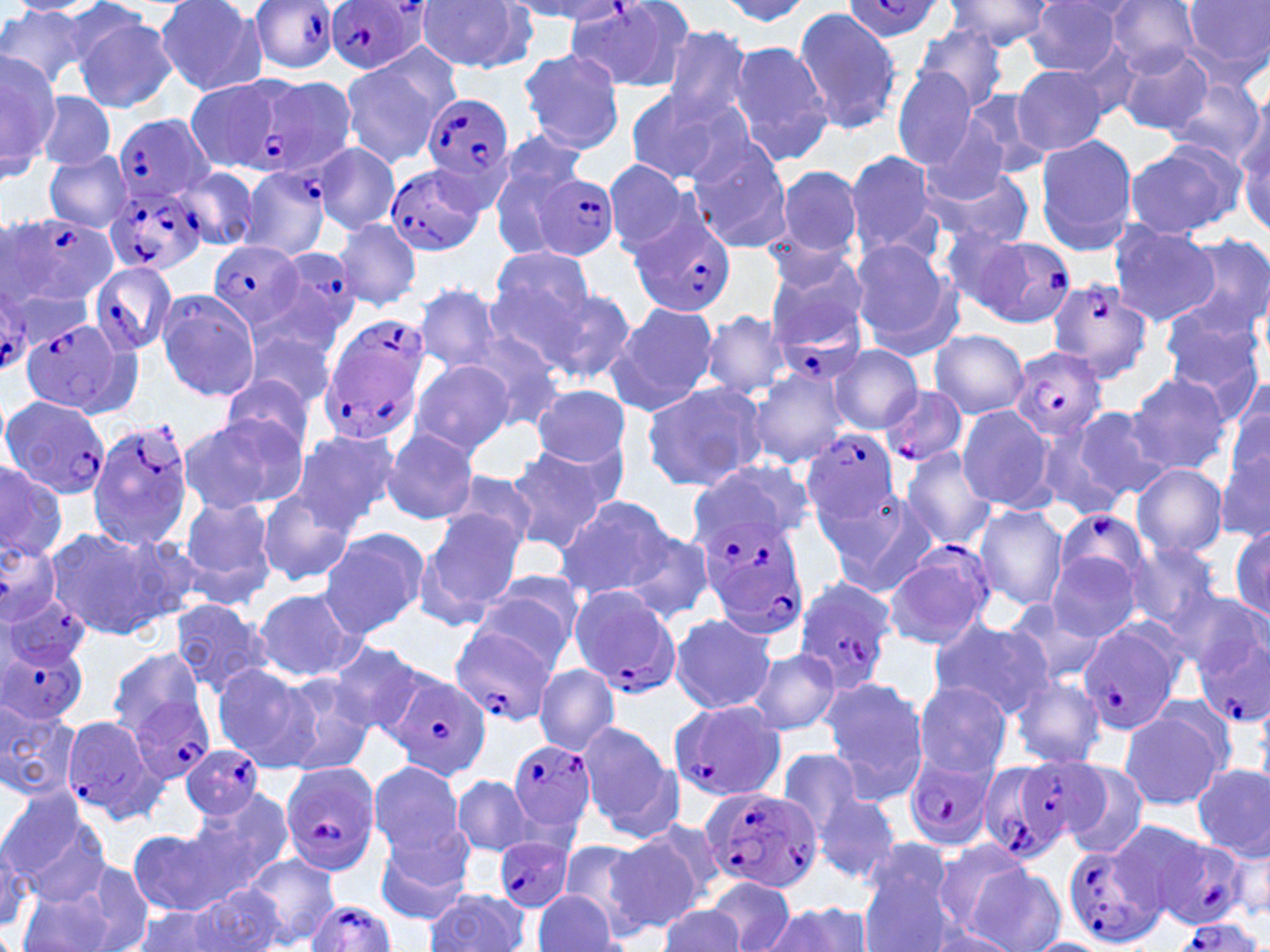
Summary:
  - Coordinate format: approximate bounding boxes as [x1, y1, x2, y2] in pixels
  - Plasmodium falciparum-infected red blood cell locations (subset): [568, 0, 699, 94], [247, 1, 342, 73], [325, 1, 426, 76], [842, 1, 946, 40], [221, 77, 317, 181], [423, 93, 513, 190], [110, 114, 217, 201], [386, 162, 488, 257], [239, 165, 332, 261], [534, 173, 621, 261], [101, 186, 203, 276], [630, 209, 735, 318], [10, 214, 117, 305], [951, 232, 1073, 326], [208, 241, 304, 331], [261, 246, 363, 353], [90, 262, 179, 356], [1045, 276, 1156, 383], [0, 286, 39, 370], [771, 298, 866, 385], [20, 319, 128, 418], [319, 325, 431, 445], [1009, 347, 1107, 442], [881, 385, 967, 466], [1, 397, 112, 501], [88, 418, 195, 551], [800, 429, 899, 529], [1056, 507, 1153, 598], [697, 510, 808, 623], [884, 540, 994, 650], [0, 543, 63, 624], [794, 581, 899, 690], [567, 584, 686, 699], [1, 590, 91, 671], [1079, 621, 1184, 736], [450, 625, 557, 728], [0, 632, 89, 723], [383, 669, 492, 782], [125, 694, 217, 784], [666, 701, 786, 803], [58, 715, 167, 824], [506, 737, 597, 834], [180, 744, 264, 820], [903, 756, 997, 850], [980, 756, 1089, 864], [278, 761, 382, 876], [700, 786, 823, 897], [1150, 824, 1238, 929], [493, 835, 575, 914], [1060, 842, 1161, 949], [306, 899, 397, 952], [1168, 918, 1266, 952]
  - Uninfected red blood cell locations (subset): [945, 0, 1056, 53], [9, 1, 98, 16], [155, 1, 267, 96], [719, 1, 812, 27], [418, 2, 536, 73], [505, 2, 628, 22], [1103, 2, 1203, 74], [1181, 2, 1270, 79], [1022, 3, 1128, 76], [0, 5, 98, 92], [793, 7, 899, 136], [72, 11, 178, 112], [911, 23, 1010, 114], [659, 26, 755, 126], [728, 41, 833, 167], [516, 47, 627, 154], [1117, 47, 1214, 136], [0, 51, 56, 173], [340, 54, 453, 167], [1011, 62, 1113, 158], [892, 66, 979, 170], [183, 76, 263, 172], [289, 76, 357, 174], [1164, 77, 1267, 167], [623, 88, 747, 187], [960, 88, 1050, 180], [38, 92, 116, 171], [1236, 117, 1269, 235], [919, 121, 1011, 205], [1034, 134, 1137, 254], [685, 137, 793, 253], [1123, 142, 1245, 238], [313, 143, 401, 235], [845, 149, 943, 261], [44, 152, 133, 231], [601, 158, 698, 258], [177, 165, 260, 253], [774, 165, 863, 261], [924, 168, 1037, 248], [334, 218, 420, 310], [1108, 222, 1217, 326], [1177, 234, 1270, 337], [850, 240, 964, 360], [486, 247, 600, 348], [764, 253, 869, 345], [414, 283, 503, 373], [538, 285, 638, 386], [156, 291, 261, 401], [1160, 299, 1266, 405], [607, 302, 719, 417], [699, 311, 791, 398], [243, 328, 339, 413], [929, 329, 1028, 419], [467, 332, 567, 432], [830, 345, 925, 434], [408, 358, 516, 455], [1126, 372, 1233, 475], [215, 373, 317, 465], [746, 374, 849, 467], [1226, 374, 1270, 476], [640, 380, 768, 491], [531, 384, 633, 470], [956, 405, 1055, 512], [1072, 406, 1173, 504], [179, 415, 301, 516], [1034, 417, 1131, 522], [286, 429, 395, 534], [381, 429, 480, 525], [503, 443, 619, 553], [1215, 443, 1268, 545], [877, 447, 994, 630], [900, 448, 997, 551], [692, 459, 814, 546], [1132, 462, 1229, 559], [0, 465, 67, 562], [436, 470, 538, 555], [825, 489, 941, 599], [257, 491, 354, 586], [177, 493, 280, 607], [554, 496, 678, 600], [973, 505, 1069, 612], [419, 510, 524, 621], [1230, 523, 1270, 626], [42, 525, 181, 642], [318, 528, 428, 639], [623, 530, 715, 626], [1043, 530, 1148, 641], [1120, 542, 1223, 636], [471, 575, 582, 672], [1157, 577, 1260, 669], [251, 588, 366, 682], [167, 598, 273, 699], [1003, 599, 1110, 685], [669, 612, 776, 714], [926, 618, 1054, 716], [323, 640, 426, 737], [105, 646, 207, 739], [746, 646, 842, 738], [210, 663, 322, 774], [533, 663, 620, 754], [275, 674, 379, 778], [820, 674, 931, 805], [1009, 676, 1108, 770], [911, 681, 1013, 778], [1, 702, 80, 800], [1118, 707, 1227, 811], [577, 718, 680, 841], [777, 748, 868, 841], [368, 759, 467, 857], [1060, 762, 1149, 860], [1191, 763, 1269, 859], [450, 774, 537, 857], [183, 787, 295, 901], [812, 788, 901, 884], [1, 791, 111, 904], [634, 815, 729, 910], [126, 826, 240, 917], [374, 826, 477, 926], [1229, 828, 1270, 922], [605, 835, 704, 932], [558, 837, 669, 937], [0, 839, 32, 937], [935, 839, 1042, 940], [244, 853, 339, 948], [856, 854, 958, 951], [48, 857, 156, 952], [964, 863, 1065, 952], [705, 876, 795, 952], [186, 883, 285, 952], [13, 886, 124, 952], [532, 888, 622, 952], [422, 890, 530, 951], [761, 901, 871, 952], [659, 904, 745, 952], [127, 905, 235, 950]
  - Slide-level diagnosis: Plasmodium falciparum
  - Modality: optical microscopy
  - Image size: 1270×952 pixels
  - Stain: May-Grünwald-Giemsa
  - Field of view: one of a larger specimen
  - Preparation: thin blood smear
  - Magnification: 1000x